Locate and identify every blood parasite.
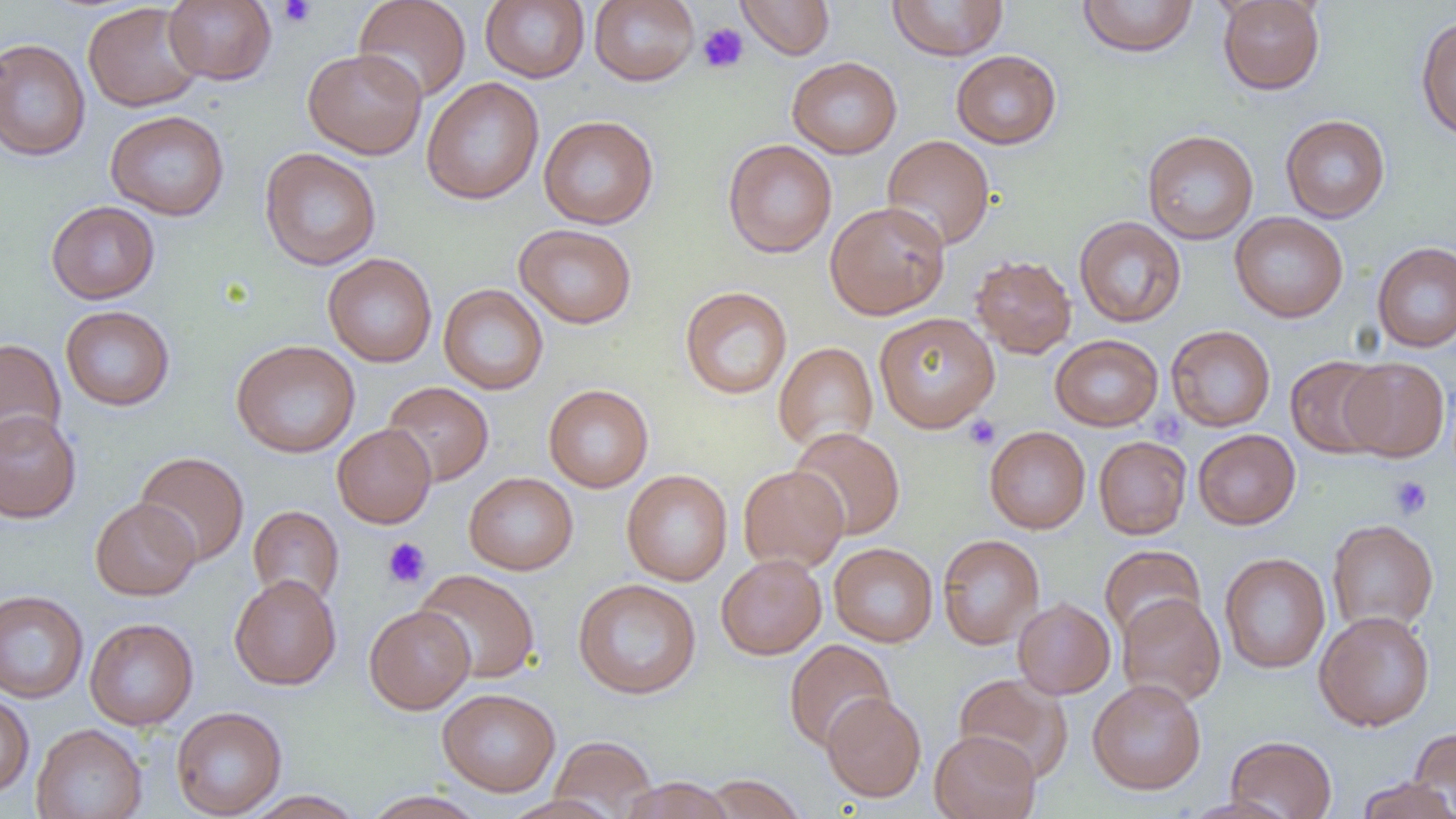

No blood parasites observed.

Approximate bounding boxes as named x1/y1/x2/y2 corners in pixels. Platelet locations: (x1=276, y1=0, x2=318, y2=28), (x1=697, y1=22, x2=749, y2=74), (x1=963, y1=415, x2=1000, y2=450), (x1=1389, y1=476, x2=1433, y2=519), (x1=382, y1=537, x2=431, y2=589). Uninfected red blood cell locations: (x1=163, y1=0, x2=277, y2=85), (x1=353, y1=0, x2=472, y2=103), (x1=480, y1=0, x2=590, y2=83), (x1=589, y1=0, x2=700, y2=86), (x1=737, y1=0, x2=835, y2=59), (x1=887, y1=0, x2=1009, y2=61), (x1=1077, y1=0, x2=1198, y2=57), (x1=1217, y1=0, x2=1325, y2=95), (x1=82, y1=2, x2=205, y2=113), (x1=1416, y1=16, x2=1456, y2=140), (x1=0, y1=37, x2=91, y2=162), (x1=302, y1=48, x2=427, y2=159), (x1=951, y1=50, x2=1061, y2=149), (x1=787, y1=56, x2=902, y2=159), (x1=421, y1=77, x2=544, y2=205), (x1=105, y1=110, x2=230, y2=221), (x1=1280, y1=114, x2=1390, y2=223), (x1=539, y1=115, x2=658, y2=229), (x1=1142, y1=129, x2=1259, y2=244), (x1=881, y1=135, x2=995, y2=251), (x1=722, y1=139, x2=837, y2=258), (x1=259, y1=147, x2=381, y2=271), (x1=46, y1=200, x2=160, y2=304), (x1=825, y1=200, x2=951, y2=320), (x1=1229, y1=212, x2=1348, y2=323), (x1=1074, y1=216, x2=1187, y2=327), (x1=513, y1=223, x2=637, y2=329), (x1=1372, y1=241, x2=1456, y2=353), (x1=322, y1=253, x2=437, y2=367), (x1=970, y1=254, x2=1077, y2=359), (x1=438, y1=283, x2=549, y2=395), (x1=679, y1=286, x2=793, y2=400), (x1=60, y1=305, x2=175, y2=411), (x1=874, y1=312, x2=1000, y2=433), (x1=1165, y1=325, x2=1275, y2=432), (x1=1050, y1=334, x2=1163, y2=431), (x1=0, y1=338, x2=66, y2=452), (x1=230, y1=339, x2=361, y2=458), (x1=773, y1=341, x2=878, y2=453), (x1=1285, y1=356, x2=1389, y2=458), (x1=1339, y1=357, x2=1450, y2=462), (x1=381, y1=381, x2=494, y2=486), (x1=543, y1=384, x2=654, y2=492), (x1=0, y1=410, x2=81, y2=523), (x1=332, y1=424, x2=436, y2=529), (x1=984, y1=426, x2=1090, y2=533), (x1=789, y1=427, x2=905, y2=540), (x1=1192, y1=429, x2=1300, y2=529), (x1=1093, y1=436, x2=1191, y2=539), (x1=134, y1=452, x2=249, y2=566), (x1=738, y1=465, x2=849, y2=572), (x1=622, y1=469, x2=733, y2=586), (x1=463, y1=472, x2=578, y2=575), (x1=90, y1=497, x2=200, y2=600), (x1=248, y1=505, x2=344, y2=606), (x1=1326, y1=519, x2=1439, y2=633), (x1=937, y1=533, x2=1045, y2=650), (x1=828, y1=543, x2=938, y2=647), (x1=1099, y1=545, x2=1206, y2=643), (x1=1219, y1=552, x2=1330, y2=674), (x1=716, y1=554, x2=827, y2=660), (x1=414, y1=568, x2=540, y2=683), (x1=229, y1=574, x2=341, y2=690), (x1=573, y1=578, x2=702, y2=699), (x1=0, y1=590, x2=89, y2=703), (x1=1116, y1=593, x2=1226, y2=706), (x1=1012, y1=598, x2=1116, y2=699), (x1=364, y1=605, x2=475, y2=714), (x1=1314, y1=610, x2=1435, y2=731), (x1=84, y1=618, x2=199, y2=730), (x1=784, y1=639, x2=895, y2=752), (x1=954, y1=673, x2=1073, y2=782), (x1=1087, y1=679, x2=1207, y2=795), (x1=437, y1=688, x2=561, y2=796), (x1=822, y1=692, x2=926, y2=802), (x1=0, y1=693, x2=34, y2=797), (x1=171, y1=706, x2=287, y2=818), (x1=31, y1=723, x2=147, y2=819), (x1=1410, y1=727, x2=1456, y2=817), (x1=929, y1=729, x2=1041, y2=819), (x1=549, y1=735, x2=657, y2=818), (x1=1225, y1=735, x2=1337, y2=818), (x1=702, y1=774, x2=808, y2=819), (x1=1357, y1=776, x2=1455, y2=819), (x1=619, y1=777, x2=736, y2=818), (x1=243, y1=790, x2=366, y2=818), (x1=361, y1=790, x2=488, y2=819), (x1=501, y1=794, x2=623, y2=819). Slide-level diagnosis: negative for blood parasites. Captured at 1000x magnification. Single field of view. Image is 1456×819 pixels. Thin blood smear. Optical microscopy.